Name the blood parasite species.
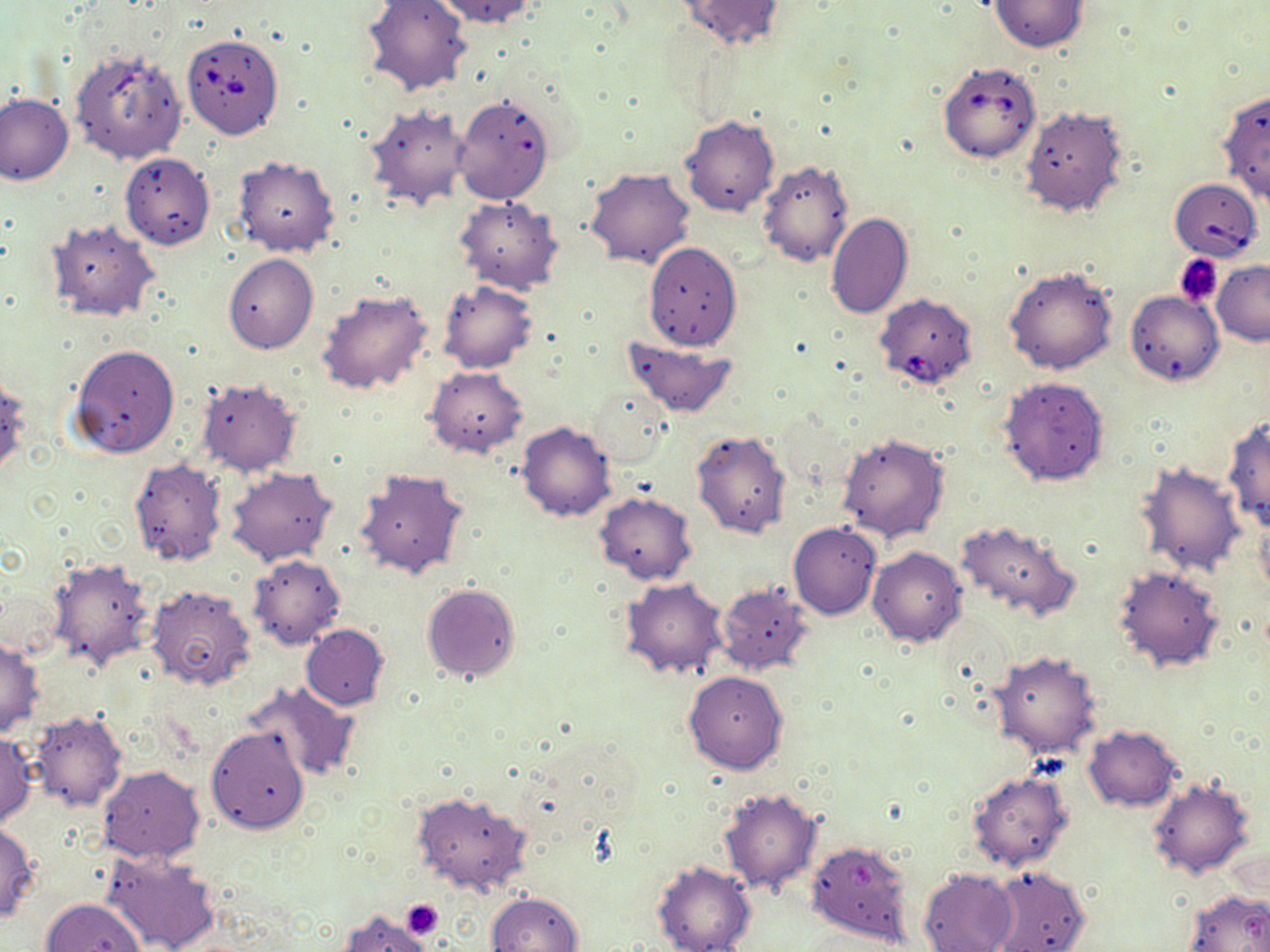

Babesia divergens.

Summary:
  - Coordinate format: approximate bounding boxes as (x1,y1)-(x2,y2) corner pairs in pixels
  - Platelet locations: (1175,255)-(1223,307), (402,898)-(444,939)
  - Babesia divergens-infected red blood cell locations: (183,34)-(282,138), (938,63)-(1041,163), (1167,176)-(1259,261), (874,293)-(977,391)
  - Uninfected red blood cell locations: (361,0)-(473,98), (436,0)-(543,28), (676,0)-(788,50), (988,0)-(1088,51), (70,48)-(187,166), (1216,89)-(1270,206), (0,94)-(74,183), (453,94)-(554,205), (363,105)-(471,211), (1021,105)-(1127,217), (680,115)-(777,218), (119,151)-(214,250), (233,157)-(339,257), (756,160)-(853,268), (584,167)-(696,269), (455,196)-(563,294), (825,212)-(913,319), (48,220)-(158,320), (644,242)-(742,351), (224,254)-(318,353), (1213,262)-(1270,345), (1004,267)-(1117,374), (439,280)-(537,373), (315,289)-(434,396), (1126,290)-(1223,385), (621,337)-(738,416), (69,343)-(180,460), (425,365)-(529,458), (998,375)-(1109,486), (0,376)-(29,480), (197,378)-(301,475), (587,386)-(672,469), (1223,415)-(1270,533), (517,422)-(615,522), (692,429)-(791,538), (837,431)-(949,542), (128,458)-(228,567), (1136,461)-(1245,576), (223,466)-(337,567), (355,468)-(468,581), (594,492)-(698,584), (1253,509)-(1270,601), (955,520)-(1082,622), (788,521)-(882,620), (868,548)-(966,648), (247,555)-(345,650), (49,557)-(154,670), (1112,564)-(1224,671), (619,578)-(728,680), (422,583)-(520,681), (717,584)-(813,677), (147,585)-(256,692), (301,624)-(388,709), (0,639)-(44,737), (990,651)-(1102,759), (684,670)-(788,774), (241,680)-(359,782), (26,711)-(128,811), (1083,725)-(1181,811), (206,727)-(309,834), (0,733)-(37,827), (99,766)-(205,863), (967,771)-(1074,871), (1148,779)-(1254,879), (716,786)-(824,894), (411,791)-(532,897), (0,822)-(40,922), (805,839)-(916,948), (104,849)-(221,952), (652,860)-(756,952), (985,865)-(1090,952), (918,867)-(1020,952), (1184,890)-(1270,952), (485,892)-(582,952), (42,897)-(144,952), (338,909)-(436,952)
  - Modality: optical microscopy
  - Magnification: 1000x
  - Preparation: thin blood film
  - Image size: 1270×952 pixels
  - Field of view: single
  - Stain: May-Grünwald-Giemsa